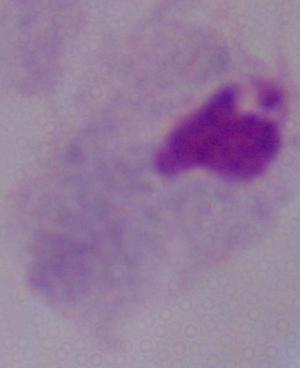
A trichomonad is seen. Photomicrograph. Captured at 1000x magnification.